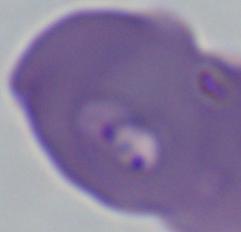 Captured at 1000x magnification. Photomicrograph. A Babesia parasite is shown.